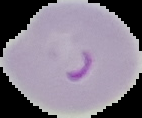 From a thin blood smear. The area outside the segmented cell region is set to black. Malaria status: parasitized. Image is 142×118 pixels.